Assess this cell for malaria.
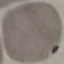
Uninfected.

stain: Giemsa
image_type: automatically extracted cell patch, resized to 64 × 64 pixels
preparation: thin blood film
capture: smartphone camera at the microscope eyepiece